Comment on the morphology of the red blood cells.
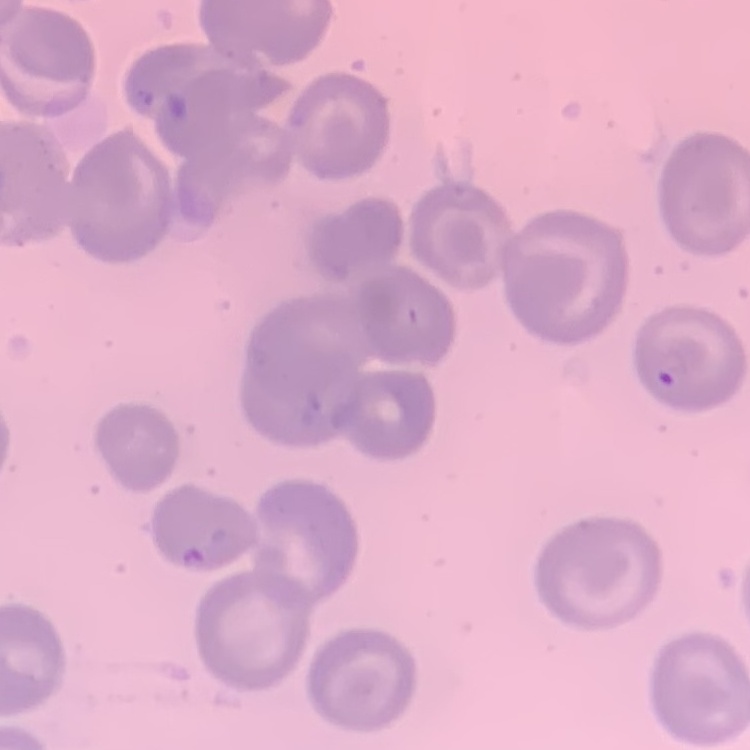

They show no rouleaux formation.

Square crop of a larger photomicrograph. Thin blood film. Field's or Giemsa stain.